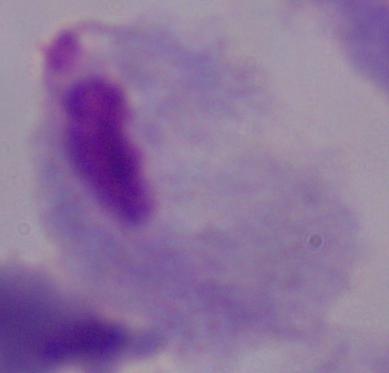

identification: trichomonad
modality: photomicrograph
magnification: 1000x